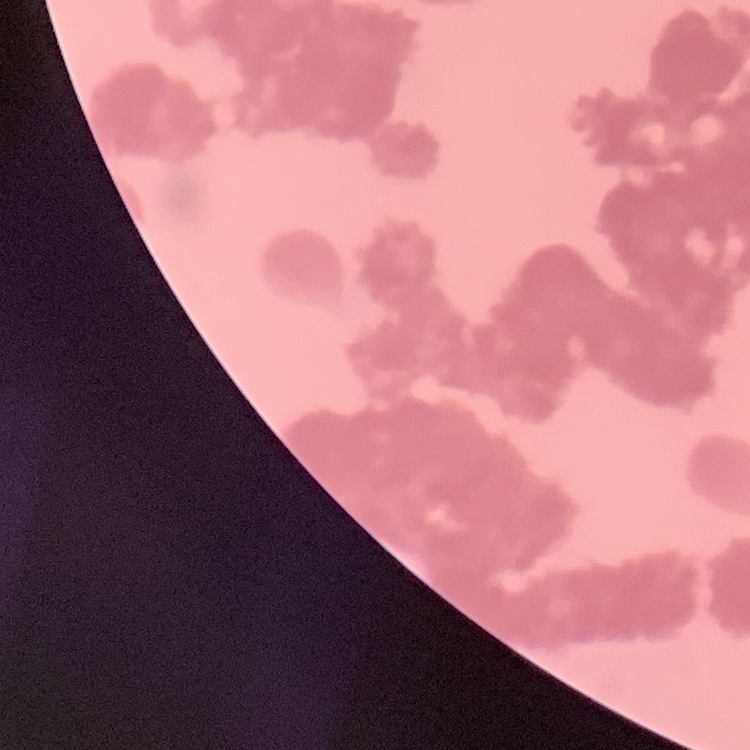
The erythrocytes exhibit rouleaux formation. Field's or Giemsa stain. Thin blood film. Square crop of a larger photomicrograph.